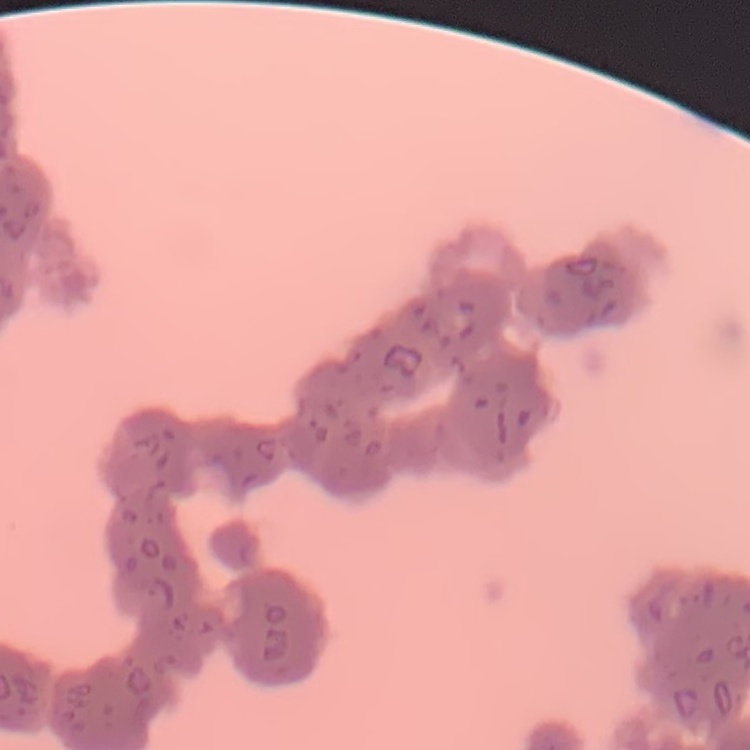

Summary:
  - Red blood cell morphology: rouleaux formation
  - Preparation: thin peripheral smear
  - Image type: one tile cut from a larger photomicrograph
  - Stain: Field's or Giemsa